Classify this cell by malaria status.
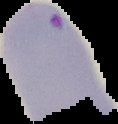
Parasitized.

Segmented cell region on a black background. Image is 118×124 pixels. From a thin blood smear.